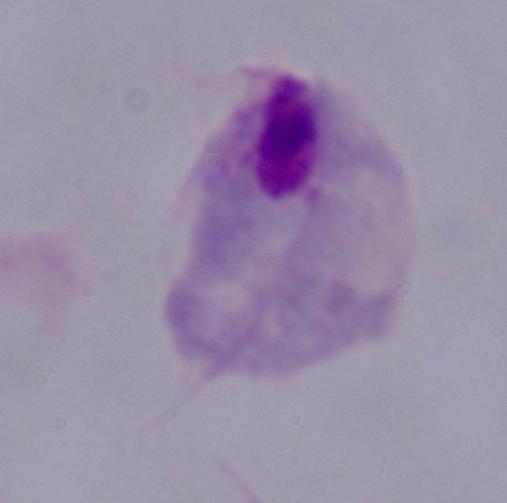

modality = micrograph
identification = trichomonad
magnification = 1000x